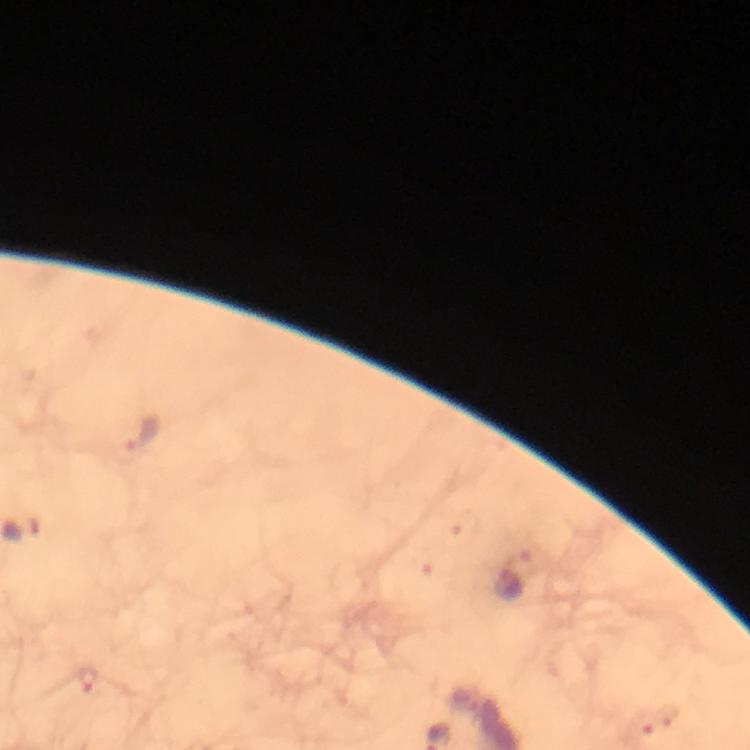
Approximate centers as [x, y] in pixels. Malaria parasite locations: [513, 574], [89, 679], [646, 721]. Thick blood film. Cropped region of a single field of view. At 100x magnification. Image is 750×750 pixels. Giemsa-stained preparation. Photographed through the microscope with a smartphone camera. Immersion oil applied. From a diagnostic examination for malaria.